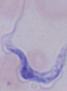
{
  "identification": "trypanosome",
  "modality": "micrograph",
  "magnification": "1000x"
}